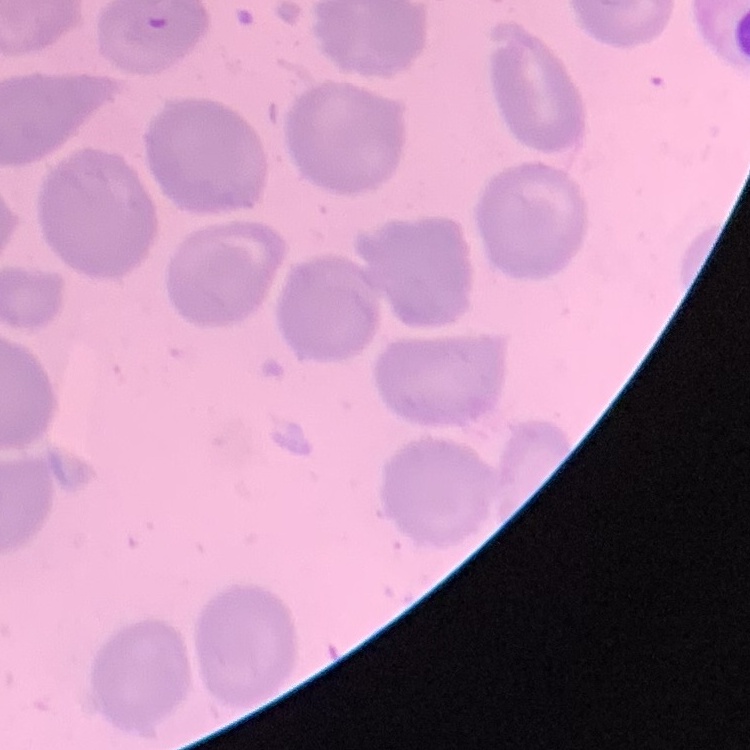

Summary:
  - Erythrocyte morphology: no rouleaux formation
  - Stain: Field's or Giemsa
  - Preparation: thin peripheral smear
  - Image type: one tile cut from a larger photomicrograph